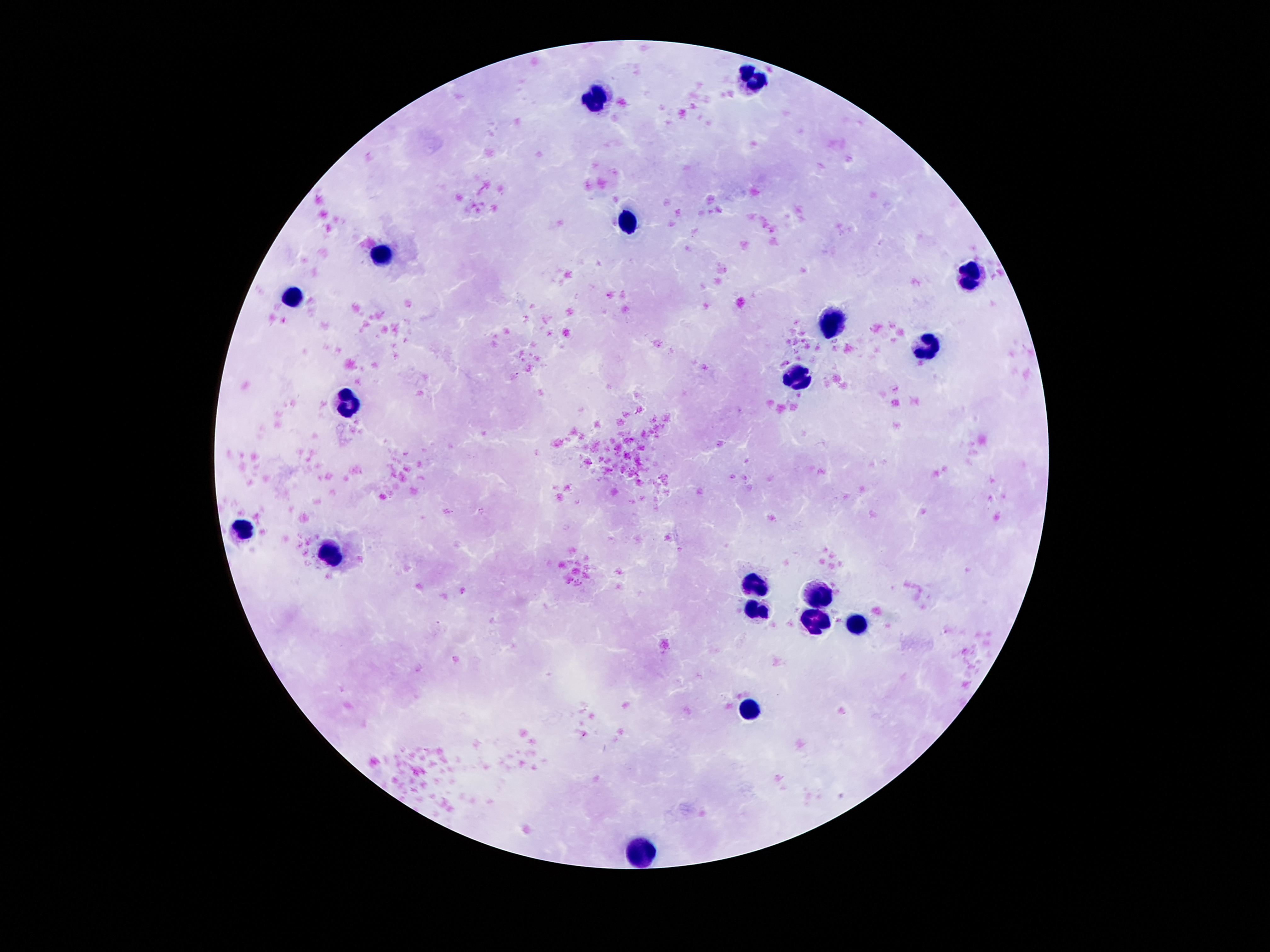

Approximate centers as [x, y] in pixels.
Summary:
  - Leukocyte locations: [752, 80], [597, 104], [630, 221], [385, 256], [969, 274], [294, 301], [832, 320], [927, 345], [796, 378], [343, 406], [241, 528], [332, 551], [752, 584], [819, 598], [754, 610], [812, 621], [858, 624], [750, 705], [642, 851]
  - Capture: smartphone camera through the microscope eyepiece
  - Magnification: 100x
  - Image size: 1270×952 pixels
  - Patient malaria status: not infected
  - Preparation: thick blood smear
  - Stain: Giemsa
  - Field of view: single